Name the blood parasite species.
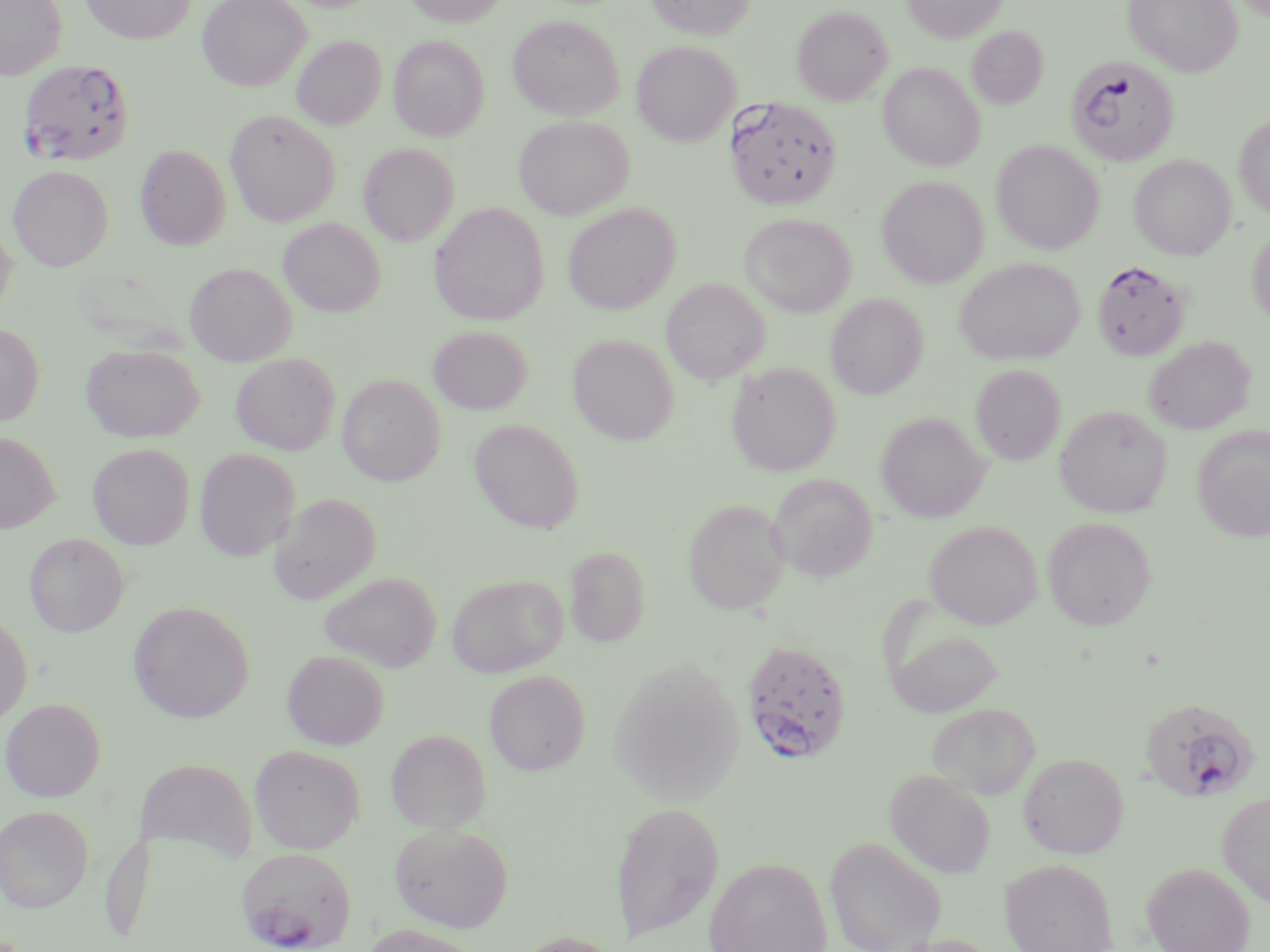

Plasmodium falciparum.

{
  "uninfected_red_blood_cell_locations": "approximate bounding boxes as (x1, y1, x2, y2) in pixels: (0, 0, 68, 79), (79, 0, 197, 44), (198, 0, 311, 91), (402, 0, 509, 27), (647, 0, 755, 40), (902, 0, 1006, 42), (1124, 0, 1242, 76), (792, 6, 892, 105), (507, 15, 624, 119), (967, 26, 1048, 109), (389, 35, 489, 141), (292, 36, 386, 130), (632, 41, 740, 146), (878, 63, 985, 171), (225, 109, 341, 227), (515, 116, 634, 219), (1233, 116, 1270, 218), (991, 140, 1104, 254), (358, 143, 459, 246), (135, 144, 231, 250), (1129, 154, 1236, 260), (8, 165, 113, 270), (876, 175, 988, 288), (429, 202, 549, 325), (562, 203, 680, 314), (739, 213, 856, 317), (0, 217, 18, 317), (279, 218, 385, 317), (1247, 226, 1270, 324), (954, 257, 1084, 365), (185, 262, 297, 366), (661, 277, 770, 384), (825, 293, 928, 399), (0, 322, 44, 426), (428, 326, 533, 414), (568, 333, 680, 445), (1144, 335, 1255, 434), (81, 344, 204, 442), (230, 353, 340, 455), (726, 361, 840, 476), (970, 364, 1066, 465), (338, 374, 445, 486), (1054, 405, 1172, 517), (876, 411, 990, 523), (470, 419, 584, 533), (1192, 427, 1270, 540), (0, 431, 61, 533), (88, 443, 195, 549), (195, 448, 299, 561), (769, 473, 878, 581), (269, 493, 381, 603), (683, 498, 791, 614), (1042, 516, 1157, 631), (924, 520, 1042, 629), (24, 533, 129, 637), (565, 546, 650, 647), (318, 571, 442, 672), (446, 574, 567, 677), (128, 600, 255, 723), (0, 613, 32, 726), (886, 626, 1005, 717), (282, 649, 389, 749), (608, 657, 745, 806), (484, 670, 590, 775), (1, 697, 106, 802), (926, 703, 1040, 799), (386, 729, 491, 832), (249, 744, 365, 854), (1018, 752, 1129, 858), (136, 757, 258, 864), (885, 769, 996, 877), (1217, 792, 1270, 906), (610, 802, 724, 944), (0, 805, 93, 912), (389, 822, 514, 933), (824, 835, 947, 952), (703, 856, 833, 952), (1000, 858, 1118, 952), (1141, 862, 1255, 952), (359, 923, 485, 952), (509, 930, 627, 952)",
  "preparation": "thin blood smear",
  "stain": "May-Grünwald-Giemsa",
  "image_size": "1270×952 pixels",
  "plasmodium_falciparum_infected_red_blood_cell_locations": "approximate bounding boxes as (x1, y1, x2, y2) in pixels: (1066, 56, 1179, 167), (18, 59, 134, 166), (725, 96, 843, 212), (1093, 261, 1189, 361), (740, 639, 854, 765), (1140, 698, 1259, 803), (236, 846, 357, 950)",
  "modality": "optical microscopy",
  "field_of_view": "single",
  "magnification": "1000x"
}